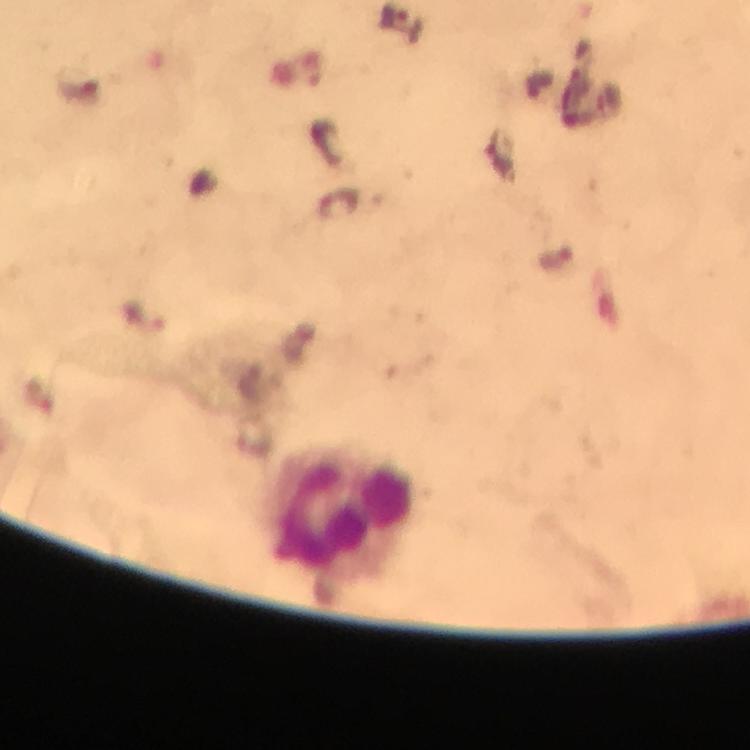

magnification = 100x
image size = 750×750 pixels
malaria parasite locations = approximate centers as {x, y} in pixels: {395, 17}
immersion oil = used
leukocyte locations = approximate centers as {x, y} in pixels: {343, 514}
cropped from = a single field of view
capture = smartphone photograph through a microscope
preparation = thick blood smear
context = from a malaria diagnostic workup
stain = Giemsa